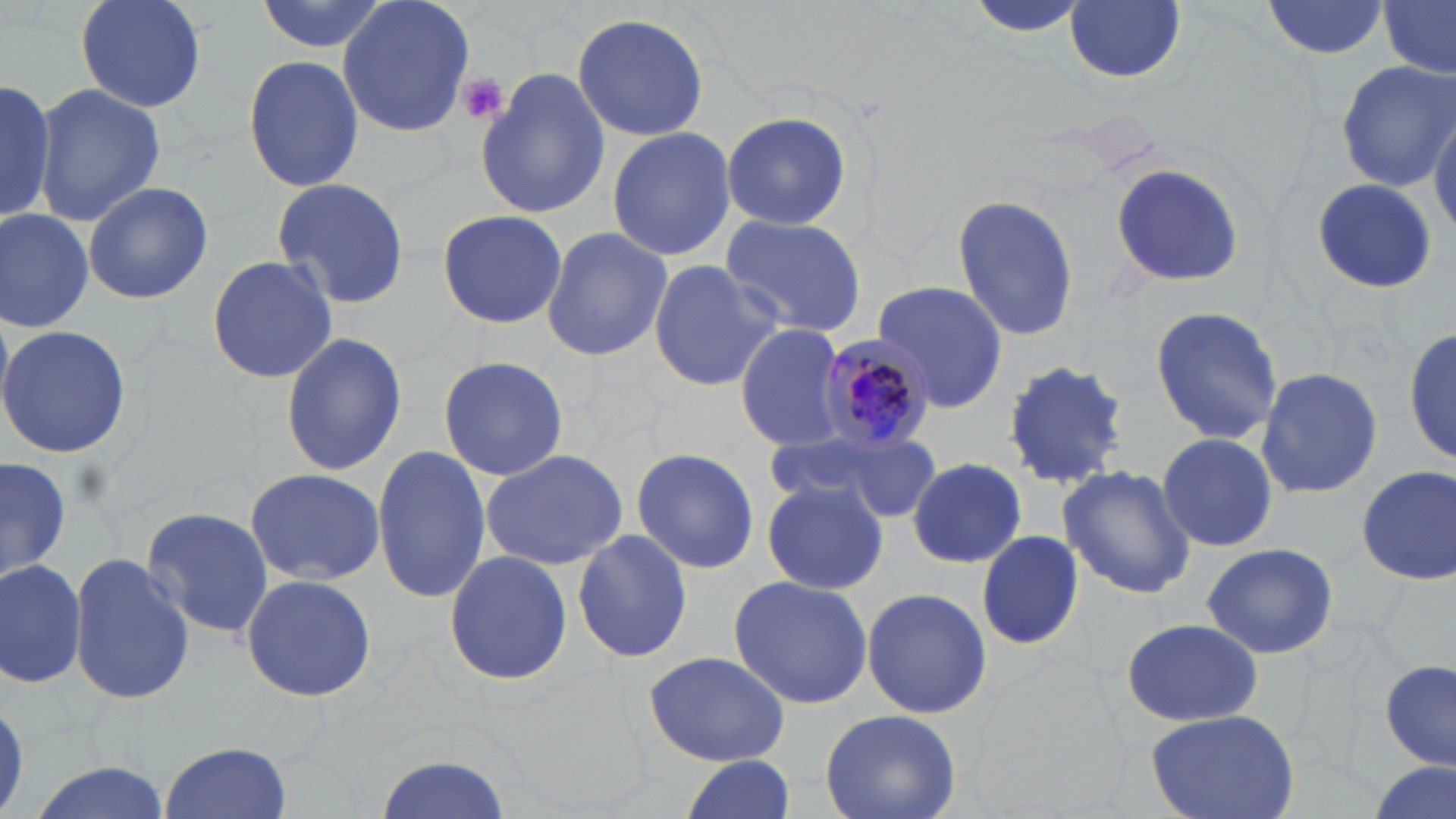

Approximate bounding boxes as (x1,y1)-(x2,y2) corner pairs in pixels. Uninfected red blood cell locations: (76,0)-(206,114), (253,0)-(393,56), (337,0)-(476,139), (967,0)-(1090,41), (1065,1)-(1187,83), (1260,1)-(1391,60), (1380,2)-(1455,80), (572,11)-(711,141), (241,54)-(365,195), (1335,63)-(1454,188), (478,66)-(610,220), (0,75)-(58,225), (34,82)-(164,226), (1430,109)-(1456,233), (720,112)-(853,231), (606,125)-(735,262), (1106,161)-(1245,288), (269,176)-(409,311), (83,179)-(214,305), (1310,179)-(1435,292), (950,193)-(1079,345), (0,208)-(95,334), (435,208)-(567,329), (719,213)-(868,335), (540,226)-(671,362), (206,254)-(336,385), (647,259)-(782,393), (876,279)-(1011,411), (1148,303)-(1283,446), (0,323)-(130,460), (735,323)-(847,452), (1407,324)-(1455,469), (279,332)-(407,476), (437,354)-(569,482), (1000,355)-(1132,487), (1256,367)-(1385,500), (771,428)-(941,521), (1156,431)-(1278,553), (371,443)-(490,607), (480,446)-(629,571), (631,448)-(760,575), (1,455)-(70,589), (907,458)-(1026,568), (1059,463)-(1195,598), (1355,466)-(1454,585), (244,467)-(385,584), (760,479)-(888,596), (142,503)-(273,641), (975,529)-(1084,649), (572,530)-(693,664), (1202,540)-(1339,660), (443,548)-(573,686), (70,552)-(193,707), (0,557)-(86,689), (240,572)-(380,702), (728,574)-(874,710), (861,587)-(992,720), (1120,617)-(1264,728), (642,650)-(791,766), (1381,659)-(1455,770), (1144,707)-(1301,819), (819,709)-(962,819), (159,741)-(293,818), (376,749)-(513,819), (676,756)-(798,819), (24,758)-(173,819), (1363,761)-(1453,819). Platelet locations: (455,73)-(509,125). Plasmodium malariae-infected red blood cell locations: (819,335)-(934,456). Slide-level diagnosis: Plasmodium malariae. Optical microscopy. One field of a larger specimen. Thin blood film. Image is 1456×819 pixels. May-Grünwald-Giemsa-stained preparation. 1000x magnification.